Locate and identify every blood parasite.
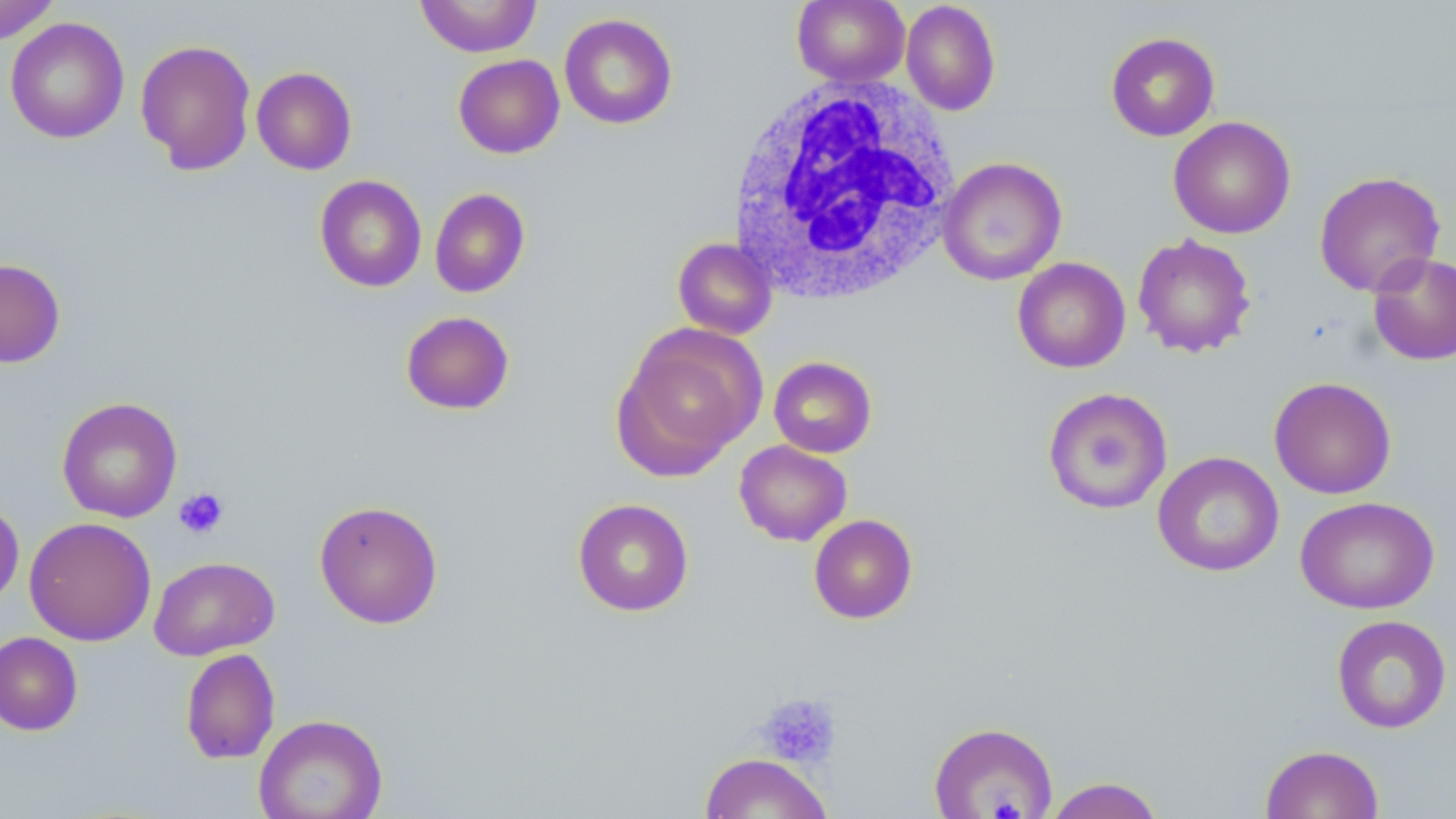

No blood parasites seen.

Approximate bounding boxes as named x1/y1/x2/y2 corners in pixels. Uninfected red blood cell locations: (x1=0, y1=0, x2=62, y2=45), (x1=414, y1=0, x2=542, y2=57), (x1=791, y1=0, x2=910, y2=87), (x1=900, y1=1, x2=1001, y2=116), (x1=559, y1=13, x2=678, y2=129), (x1=5, y1=16, x2=129, y2=144), (x1=1105, y1=31, x2=1220, y2=142), (x1=134, y1=38, x2=257, y2=175), (x1=453, y1=54, x2=564, y2=158), (x1=251, y1=66, x2=357, y2=175), (x1=1168, y1=117, x2=1296, y2=239), (x1=938, y1=157, x2=1067, y2=286), (x1=1314, y1=171, x2=1445, y2=297), (x1=314, y1=175, x2=427, y2=292), (x1=429, y1=188, x2=530, y2=298), (x1=1132, y1=233, x2=1256, y2=358), (x1=672, y1=237, x2=777, y2=340), (x1=1367, y1=251, x2=1456, y2=366), (x1=1012, y1=257, x2=1131, y2=373), (x1=0, y1=258, x2=66, y2=368), (x1=400, y1=311, x2=515, y2=415), (x1=611, y1=325, x2=764, y2=480), (x1=768, y1=356, x2=877, y2=458), (x1=1269, y1=376, x2=1397, y2=499), (x1=1042, y1=387, x2=1173, y2=514), (x1=56, y1=396, x2=183, y2=523), (x1=734, y1=440, x2=852, y2=546), (x1=1152, y1=451, x2=1284, y2=577), (x1=1295, y1=496, x2=1440, y2=615), (x1=0, y1=497, x2=24, y2=611), (x1=572, y1=498, x2=694, y2=617), (x1=314, y1=499, x2=444, y2=629), (x1=809, y1=514, x2=917, y2=624), (x1=24, y1=516, x2=157, y2=646), (x1=149, y1=556, x2=280, y2=660), (x1=1331, y1=615, x2=1452, y2=734), (x1=0, y1=632, x2=83, y2=735), (x1=180, y1=648, x2=280, y2=764), (x1=253, y1=713, x2=388, y2=818), (x1=928, y1=721, x2=1058, y2=818), (x1=1260, y1=744, x2=1384, y2=819), (x1=699, y1=752, x2=831, y2=818), (x1=1043, y1=777, x2=1166, y2=819). White blood cell locations: (x1=725, y1=78, x2=963, y2=308). Platelet locations: (x1=173, y1=487, x2=229, y2=540), (x1=756, y1=693, x2=841, y2=769), (x1=985, y1=792, x2=1035, y2=819). Slide-level diagnosis: negative for blood parasites. Thin blood film. Image is 1456×819 pixels. Single field of view. May-Grünwald-Giemsa-stained preparation. Light microscopy. 1000x magnification.